Classify this cell by malaria status.
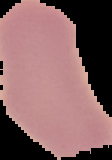

Uninfected.

Summary:
  - Preparation: thin blood film
  - Image size: 112×160 pixels
  - Image type: segmented cell region with the area outside set to black